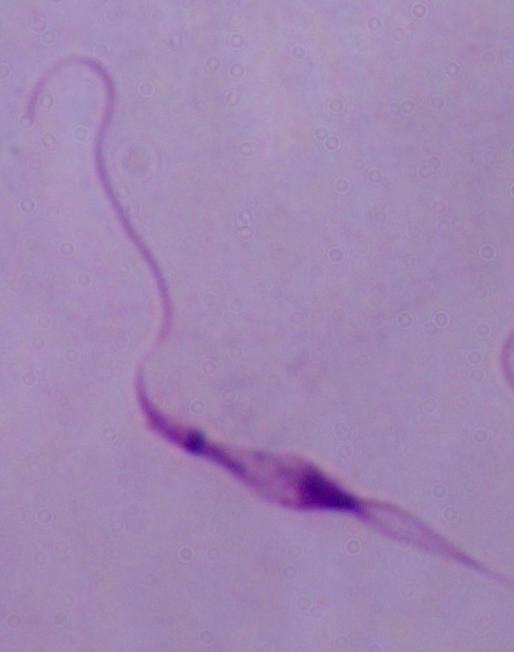
Micrograph. A Leishmania parasite is shown. Captured at 1000x magnification.